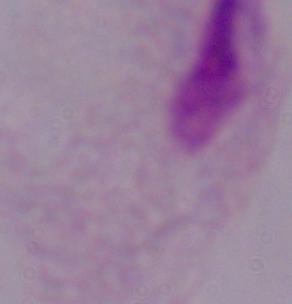
Summary:
  - Modality: photomicrograph
  - Magnification: 1000x
  - Identification: trichomonad